Locate every blood parasite and identify its species.
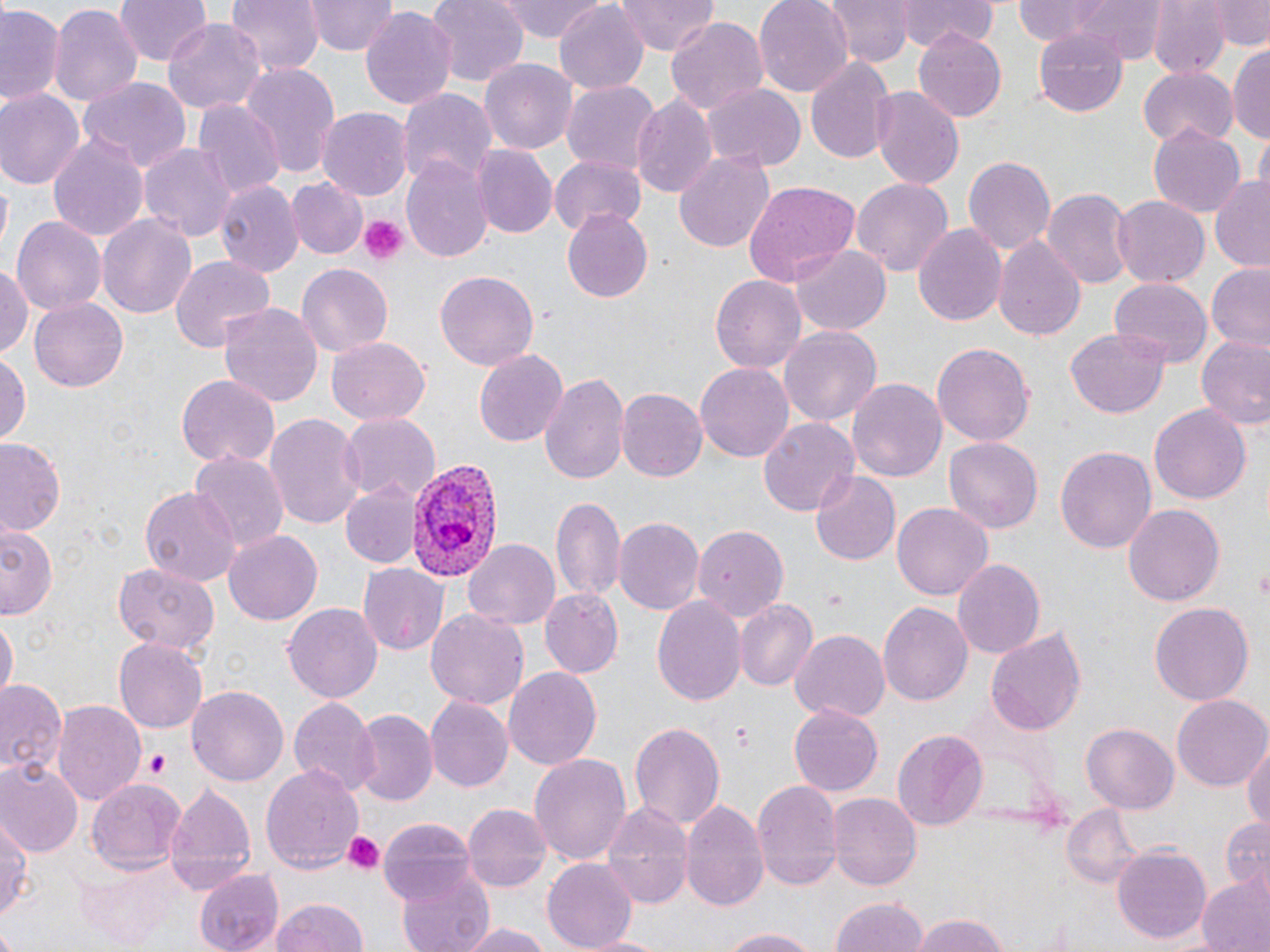

Approximate bounding boxes as (x1, y1, x2, y2) in pixels.
Plasmodium vivax-infected red blood cells: (401, 455, 502, 580).
No Plasmodium falciparum, Plasmodium ovale, Plasmodium malariae, Babesia divergens, or Trypanosoma brucei observed.

{
  "slide_level_diagnosis": "Plasmodium vivax",
  "preparation": "thin blood film",
  "magnification": "1000x",
  "platelet_locations": "approximate bounding boxes as (x1, y1, x2, y2) in pixels: (357, 215, 409, 265), (142, 750, 172, 779), (338, 830, 385, 877)",
  "modality": "optical microscopy",
  "uninfected_red_blood_cell_locations": "approximate bounding boxes as (x1, y1, x2, y2) in pixels: (224, 0, 322, 78), (308, 0, 399, 56), (425, 0, 527, 88), (493, 0, 609, 44), (617, 0, 720, 56), (755, 0, 851, 96), (821, 0, 914, 69), (898, 0, 997, 50), (1011, 0, 1165, 57), (1204, 0, 1270, 48), (112, 1, 212, 68), (552, 2, 649, 91), (0, 3, 66, 109), (48, 3, 144, 108), (1147, 3, 1226, 79), (359, 7, 458, 114), (665, 15, 771, 115), (164, 18, 266, 114), (912, 27, 1008, 123), (1031, 28, 1129, 117), (1230, 41, 1270, 148), (806, 56, 894, 164), (481, 59, 576, 155), (239, 65, 340, 184), (1138, 67, 1238, 147), (78, 77, 191, 172), (560, 80, 659, 175), (704, 83, 805, 171), (397, 86, 498, 186), (871, 86, 964, 190), (0, 89, 82, 190), (630, 92, 717, 197), (195, 100, 282, 199), (319, 107, 411, 201), (1149, 123, 1245, 220), (46, 131, 150, 244), (1252, 131, 1270, 192), (139, 143, 236, 241), (472, 144, 558, 238), (673, 149, 775, 256), (548, 153, 646, 236), (962, 153, 1055, 255), (403, 154, 492, 261), (851, 176, 953, 277), (286, 177, 369, 261), (1210, 177, 1270, 270), (216, 178, 303, 276), (742, 181, 861, 291), (1042, 185, 1133, 288), (1111, 195, 1209, 287), (561, 210, 654, 303), (97, 214, 196, 321), (12, 215, 105, 318), (914, 223, 1007, 326), (993, 235, 1087, 340), (792, 244, 893, 335), (167, 254, 276, 353), (0, 261, 33, 367), (294, 262, 393, 359), (1207, 264, 1270, 352), (436, 270, 540, 371), (711, 273, 807, 374), (1107, 279, 1212, 370), (29, 297, 129, 392), (217, 299, 323, 407), (778, 326, 882, 427), (1066, 328, 1171, 419), (1195, 334, 1270, 432), (326, 335, 432, 426), (931, 341, 1035, 447), (473, 350, 567, 446), (0, 353, 30, 442), (695, 362, 794, 462), (539, 370, 628, 483), (177, 375, 278, 473), (847, 376, 946, 481), (617, 388, 706, 483), (1149, 404, 1251, 506), (266, 413, 364, 533), (339, 415, 439, 505), (758, 415, 859, 518), (0, 438, 67, 537), (945, 438, 1042, 532), (1056, 446, 1156, 556), (189, 451, 287, 552), (809, 471, 901, 565), (342, 482, 420, 567), (138, 485, 241, 586), (552, 495, 626, 602), (893, 502, 993, 603), (1123, 503, 1225, 607), (613, 519, 703, 617), (2, 525, 59, 618), (692, 525, 787, 620), (225, 531, 322, 625), (464, 539, 561, 631), (953, 558, 1045, 659), (112, 561, 220, 658), (359, 562, 448, 656), (539, 588, 623, 678), (651, 593, 747, 706), (735, 599, 816, 692), (1149, 602, 1253, 703), (283, 603, 384, 703), (879, 603, 973, 706), (425, 609, 529, 712), (1, 620, 16, 705), (985, 626, 1088, 736), (790, 630, 890, 724), (112, 637, 208, 734), (503, 667, 601, 770), (1, 681, 64, 772), (188, 683, 290, 786), (424, 696, 513, 793), (1172, 696, 1269, 790), (289, 697, 379, 796), (52, 699, 144, 807), (788, 704, 884, 795), (352, 711, 435, 807), (628, 720, 726, 833), (1083, 722, 1179, 814), (894, 728, 986, 830), (1244, 735, 1270, 839), (528, 752, 631, 868), (0, 759, 82, 857), (261, 765, 364, 874), (753, 777, 844, 893), (85, 778, 188, 873), (163, 781, 258, 892), (827, 793, 922, 890), (600, 800, 692, 909), (680, 800, 769, 914), (462, 802, 551, 894), (1062, 803, 1147, 888), (0, 810, 32, 925), (1221, 815, 1269, 888), (379, 816, 476, 903), (1113, 844, 1212, 944), (541, 858, 640, 949), (75, 862, 181, 947), (396, 863, 496, 952), (194, 868, 285, 951), (1197, 877, 1269, 952), (830, 895, 928, 951), (268, 898, 372, 952), (909, 913, 1015, 952), (455, 922, 557, 951), (709, 926, 830, 950), (579, 933, 675, 951)",
  "stain": "May-Grünwald-Giemsa",
  "field_of_view": "one of a larger specimen",
  "image_size": "1270×952 pixels"
}